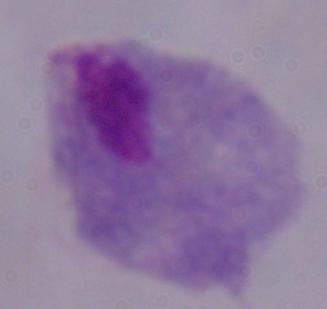

Summary:
  - Magnification: 1000x
  - Identification: trichomonad
  - Modality: micrograph